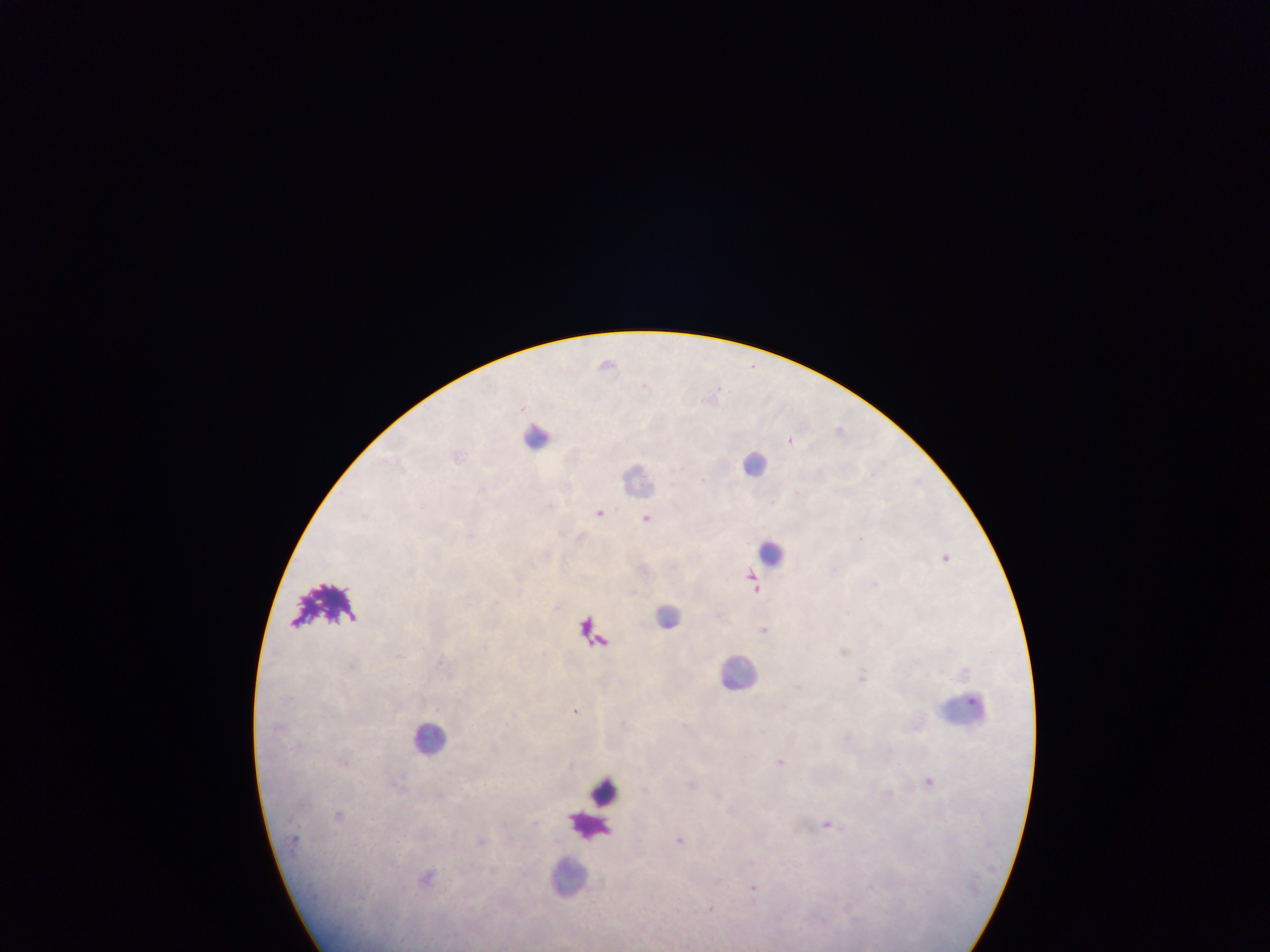

image size = 1270×952 pixels
field of view = single
country = Ghana
Plasmodium parasite locations = approximate centers as (x, y) in pixels: (606, 363), (840, 429), (791, 440), (599, 512), (364, 515), (647, 518), (860, 537), (946, 557), (835, 569), (753, 583), (875, 583), (764, 629), (863, 675), (576, 710), (781, 761), (929, 781), (828, 824), (680, 841), (753, 888)
capture = mobile-phone photograph through a microscope
leukocyte locations = approximate centers as (x, y) in pixels: (537, 432), (754, 462), (637, 479), (772, 552), (669, 616), (739, 670), (966, 709), (430, 738), (605, 792), (589, 826), (568, 878)
preparation = thick blood smear